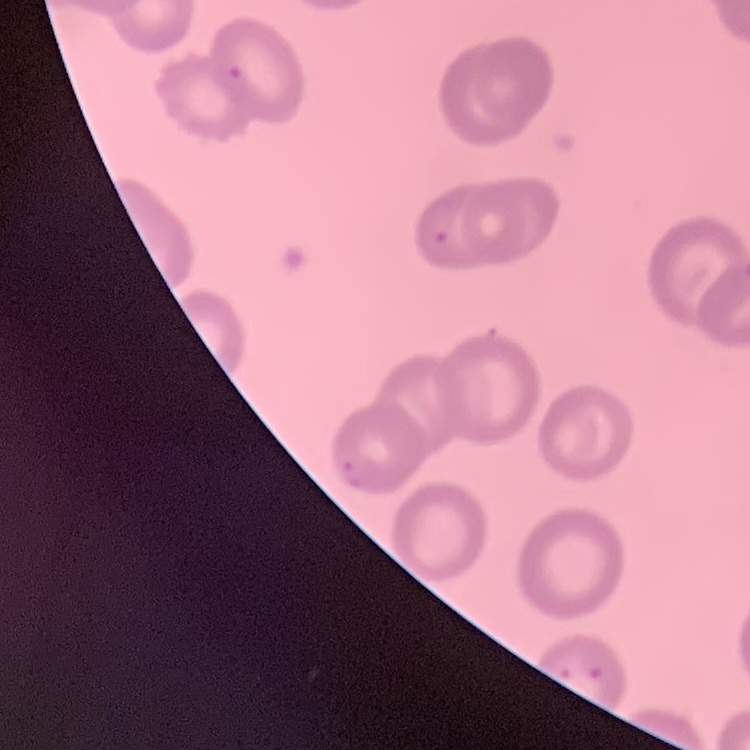

The red blood cells show no rouleaux formation. Thin blood film. One tile cut from a larger photomicrograph. Stained with either Field's or Giemsa.